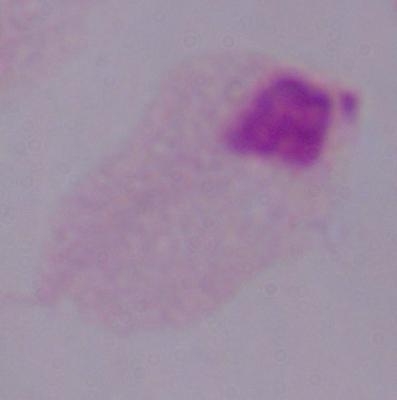
identification: trichomonad
modality: photomicrograph
magnification: 1000x